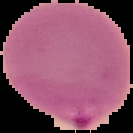

{
  "image_size": "133×133 pixels",
  "preparation": "thin blood film",
  "malaria_status": "parasitized",
  "image_type": "segmented cell region on a black background"
}